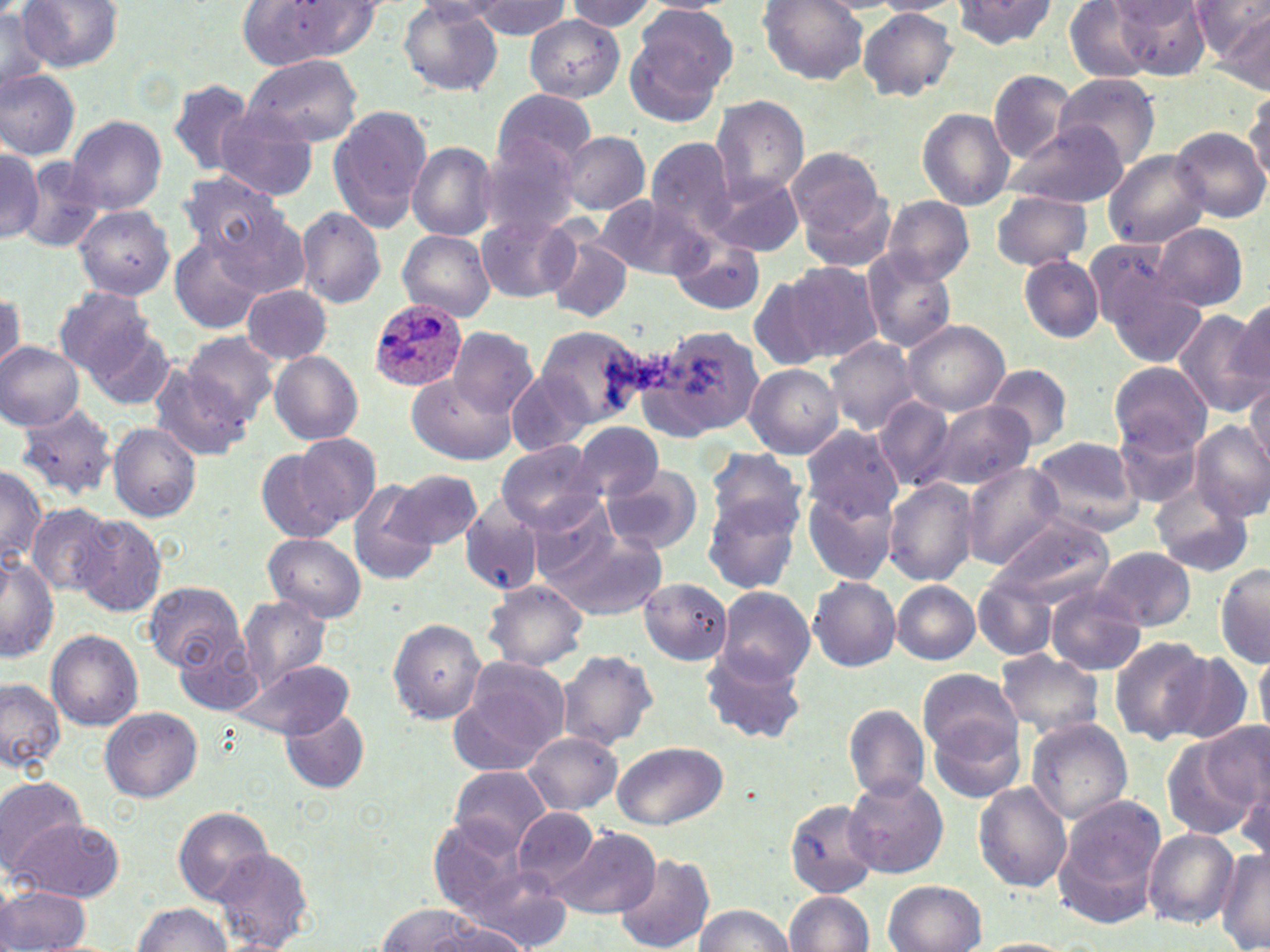
slide-level diagnosis = Plasmodium ovale
uninfected red blood cell locations = approximate bounding boxes as [x1, y1, x2, y2] in pixels: [464, 0, 569, 41], [565, 0, 660, 32], [869, 0, 963, 15], [950, 0, 1059, 50], [1191, 0, 1269, 58], [17, 1, 123, 72], [759, 1, 867, 83], [1061, 1, 1157, 83], [1110, 1, 1211, 76], [241, 2, 385, 65], [399, 3, 505, 96], [0, 5, 52, 95], [624, 6, 735, 124], [857, 7, 958, 101], [1221, 12, 1268, 94], [524, 14, 625, 101], [243, 54, 362, 147], [0, 69, 79, 159], [988, 70, 1077, 162], [1050, 73, 1160, 169], [167, 79, 255, 175], [1244, 87, 1270, 191], [491, 90, 598, 173], [710, 95, 808, 202], [328, 104, 434, 232], [211, 105, 320, 201], [917, 108, 1015, 210], [66, 116, 166, 214], [1005, 126, 1127, 210], [1171, 126, 1268, 223], [559, 131, 649, 214], [481, 136, 583, 238], [644, 137, 737, 237], [406, 141, 498, 240], [0, 146, 43, 245], [785, 148, 888, 249], [1103, 150, 1209, 249], [16, 156, 106, 254], [176, 169, 287, 261], [704, 170, 801, 258], [992, 191, 1092, 270], [595, 193, 711, 280], [881, 195, 974, 285], [72, 204, 174, 300], [295, 206, 386, 309], [219, 213, 311, 304], [476, 213, 583, 303], [1154, 224, 1248, 310], [542, 228, 635, 324], [397, 230, 496, 322], [668, 235, 766, 315], [170, 236, 263, 333], [1085, 242, 1190, 343], [861, 249, 958, 353], [1019, 255, 1104, 342], [783, 260, 882, 363], [747, 276, 832, 372], [1103, 276, 1206, 368], [242, 284, 335, 364], [54, 286, 154, 377], [1230, 298, 1270, 400], [1175, 308, 1267, 416], [902, 321, 1009, 416], [639, 324, 763, 439], [531, 325, 650, 428], [87, 326, 176, 410], [448, 326, 537, 417], [182, 332, 280, 424], [824, 337, 921, 434], [0, 342, 85, 430], [270, 350, 363, 445], [1109, 361, 1211, 453], [147, 362, 252, 462], [984, 364, 1073, 450], [743, 365, 844, 457], [507, 368, 601, 458], [407, 374, 514, 466], [1247, 377, 1270, 471], [876, 396, 953, 491], [13, 403, 121, 503], [924, 403, 1036, 492], [1115, 418, 1204, 507], [1190, 420, 1270, 522], [107, 422, 201, 523], [575, 422, 664, 502], [801, 425, 902, 521], [292, 433, 384, 529], [1029, 436, 1147, 536], [497, 440, 604, 533], [255, 444, 358, 544], [706, 446, 807, 540], [960, 462, 1066, 569], [0, 464, 45, 569], [602, 468, 701, 554], [387, 470, 481, 549], [884, 478, 980, 586], [804, 480, 900, 584], [1153, 480, 1253, 576], [347, 481, 437, 584], [703, 495, 801, 596], [459, 501, 544, 597], [528, 502, 625, 589], [28, 503, 115, 592], [74, 514, 167, 617], [988, 514, 1114, 609], [548, 526, 669, 619], [264, 533, 367, 622], [1093, 546, 1196, 632], [0, 553, 57, 663], [1215, 563, 1270, 666], [973, 575, 1058, 660], [808, 576, 900, 672], [639, 578, 730, 665], [484, 580, 588, 671], [142, 581, 245, 672], [892, 581, 980, 663], [715, 586, 815, 683], [1045, 588, 1147, 676], [237, 596, 332, 691], [388, 618, 487, 723], [46, 629, 144, 729], [172, 632, 267, 715], [1109, 636, 1210, 744], [556, 648, 658, 749], [1255, 648, 1270, 734], [701, 650, 807, 745], [995, 650, 1105, 744], [1161, 651, 1256, 745], [450, 656, 571, 773], [234, 660, 355, 740], [917, 667, 1020, 759], [0, 678, 64, 772], [843, 703, 930, 803], [279, 705, 371, 794], [100, 706, 202, 802], [929, 715, 1026, 804], [1024, 717, 1133, 825], [1204, 723, 1268, 815], [523, 732, 623, 814], [1161, 735, 1259, 840], [610, 740, 728, 830], [450, 765, 551, 854], [1, 776, 89, 874], [843, 776, 948, 879], [1237, 780, 1269, 867], [973, 783, 1071, 892], [784, 797, 882, 897], [1051, 799, 1164, 926], [172, 806, 272, 903], [511, 806, 599, 890], [10, 817, 125, 901], [430, 818, 534, 915], [551, 827, 660, 918], [1144, 829, 1240, 928], [209, 845, 315, 952], [1215, 846, 1270, 952], [613, 852, 715, 952], [457, 863, 576, 952], [883, 881, 987, 951], [0, 883, 91, 952], [785, 891, 873, 951], [131, 902, 232, 952], [376, 903, 484, 951], [694, 904, 794, 952], [429, 918, 536, 950], [975, 938, 1080, 952]
stain = May-Grünwald-Giemsa
magnification = 1000x
preparation = thin blood smear
Plasmodium ovale-infected red blood cell locations = approximate bounding boxes as [x1, y1, x2, y2] in pixels: [370, 299, 470, 392]
image size = 1270×952 pixels
field of view = single
modality = optical microscopy